Identify the preparation type.
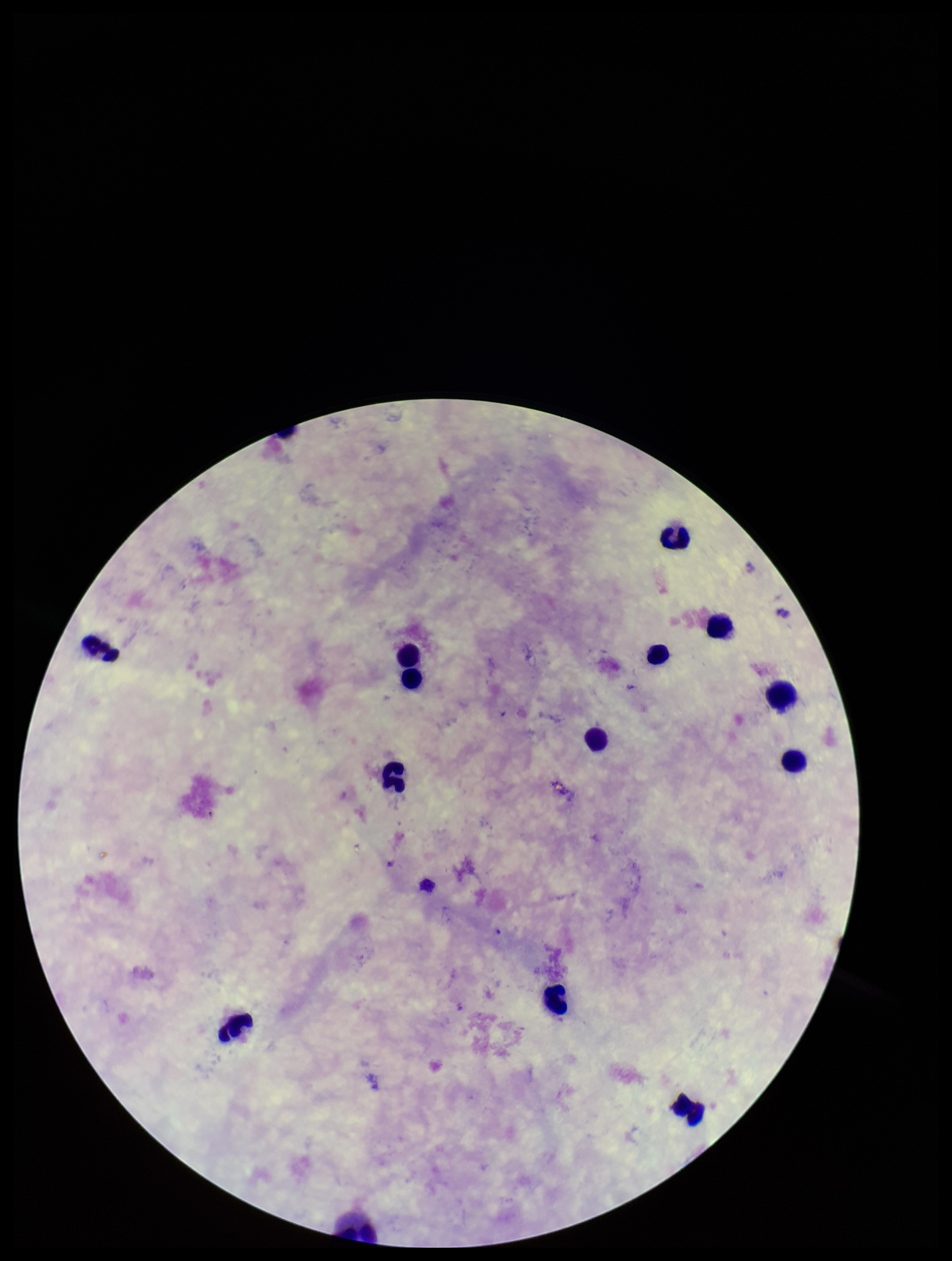

Thick.

capture = smartphone photograph through the microscope eyepiece
leukocyte count = 14
parasite count = 0
image size = 952×1261 pixels
stain = Giemsa
field of view = single
patient malaria status = negative
Plasmodium parasites = none seen